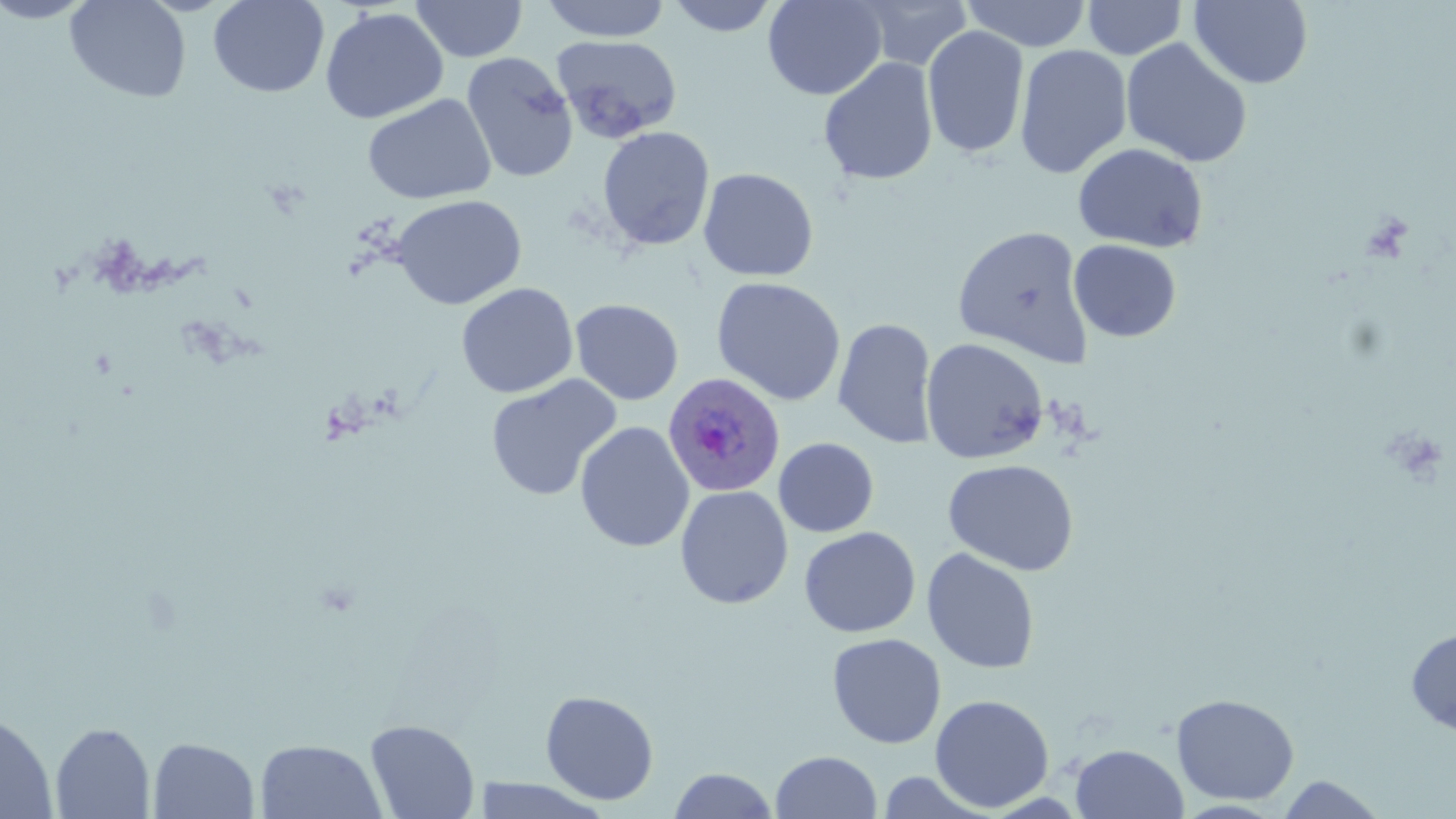

Approximate bounding boxes as (x1,y1)-(x2,y2) corner pairs in pixels. Plasmodium ovale-infected red blood cell locations: (662,372)-(786,497). Uninfected red blood cell locations: (0,0)-(98,24), (65,0)-(191,103), (208,0)-(329,98), (539,0)-(673,42), (664,0)-(782,37), (762,0)-(888,100), (857,0)-(974,71), (963,0)-(1092,51), (411,1)-(527,62), (1082,1)-(1188,60), (1189,1)-(1314,89), (320,7)-(448,124), (922,25)-(1029,159), (552,34)-(682,142), (1120,37)-(1253,168), (1014,44)-(1133,179), (460,52)-(579,182), (818,57)-(939,186), (363,94)-(496,205), (597,126)-(715,252), (1073,143)-(1208,253), (697,168)-(819,282), (391,194)-(527,310), (952,225)-(1094,367), (1069,239)-(1182,343), (711,276)-(847,406), (455,282)-(579,398), (569,298)-(684,405), (833,317)-(938,449), (920,338)-(1050,465), (486,375)-(622,501), (574,421)-(695,553), (773,437)-(879,537), (943,458)-(1079,576), (675,485)-(794,609), (799,526)-(920,638), (921,548)-(1040,674), (1405,626)-(1456,737), (827,633)-(946,749), (540,690)-(659,805), (1171,693)-(1300,805), (930,694)-(1054,812), (0,711)-(58,818), (365,718)-(480,819), (51,722)-(155,818), (147,737)-(260,818), (255,739)-(387,819), (1070,743)-(1189,818), (770,750)-(882,819), (668,767)-(779,819), (875,770)-(995,818), (1276,775)-(1389,818), (470,777)-(614,818). Slide-level diagnosis: Plasmodium ovale. May-Grünwald-Giemsa-stained preparation. Captured at 1000x magnification. Thin blood smear. Single field of view. Image is 1456×819 pixels. Light microscopy.